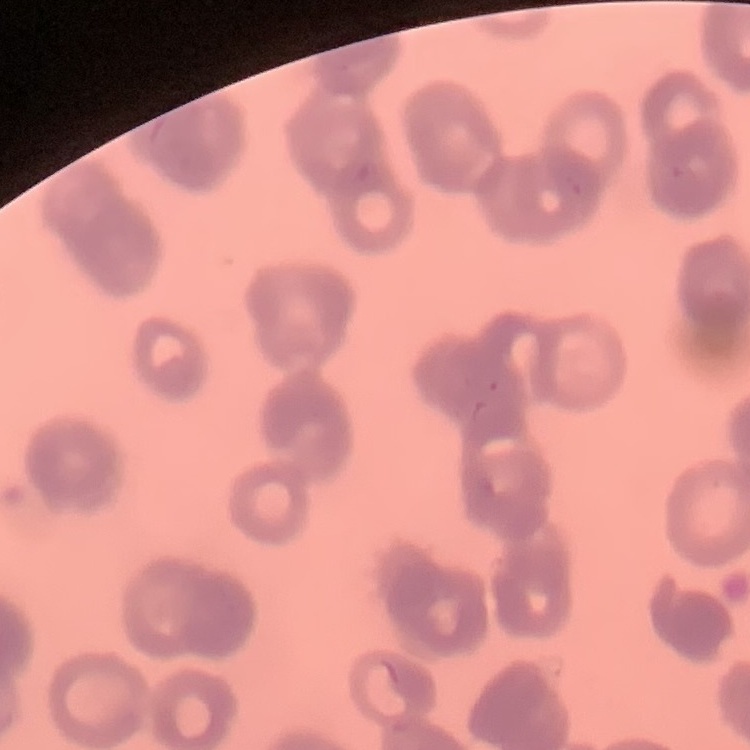 The red blood cells show rouleaux formation. Field's or Giemsa stain. Thin peripheral smear. One tile cut from a larger photomicrograph.